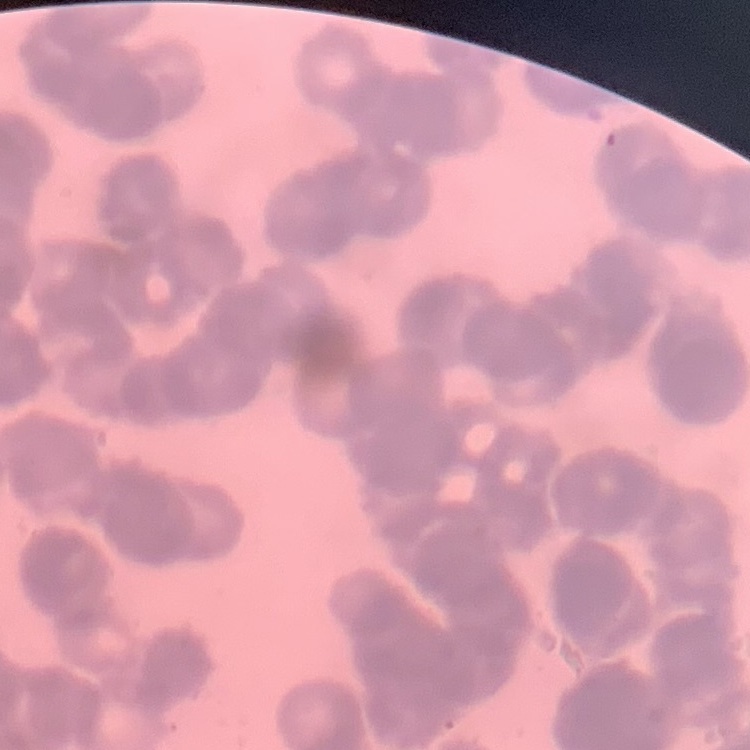

Summary:
  - Erythrocyte morphology: rouleaux formation
  - Image type: one tile cut from a larger photomicrograph
  - Preparation: thin blood film
  - Stain: Field's or Giemsa